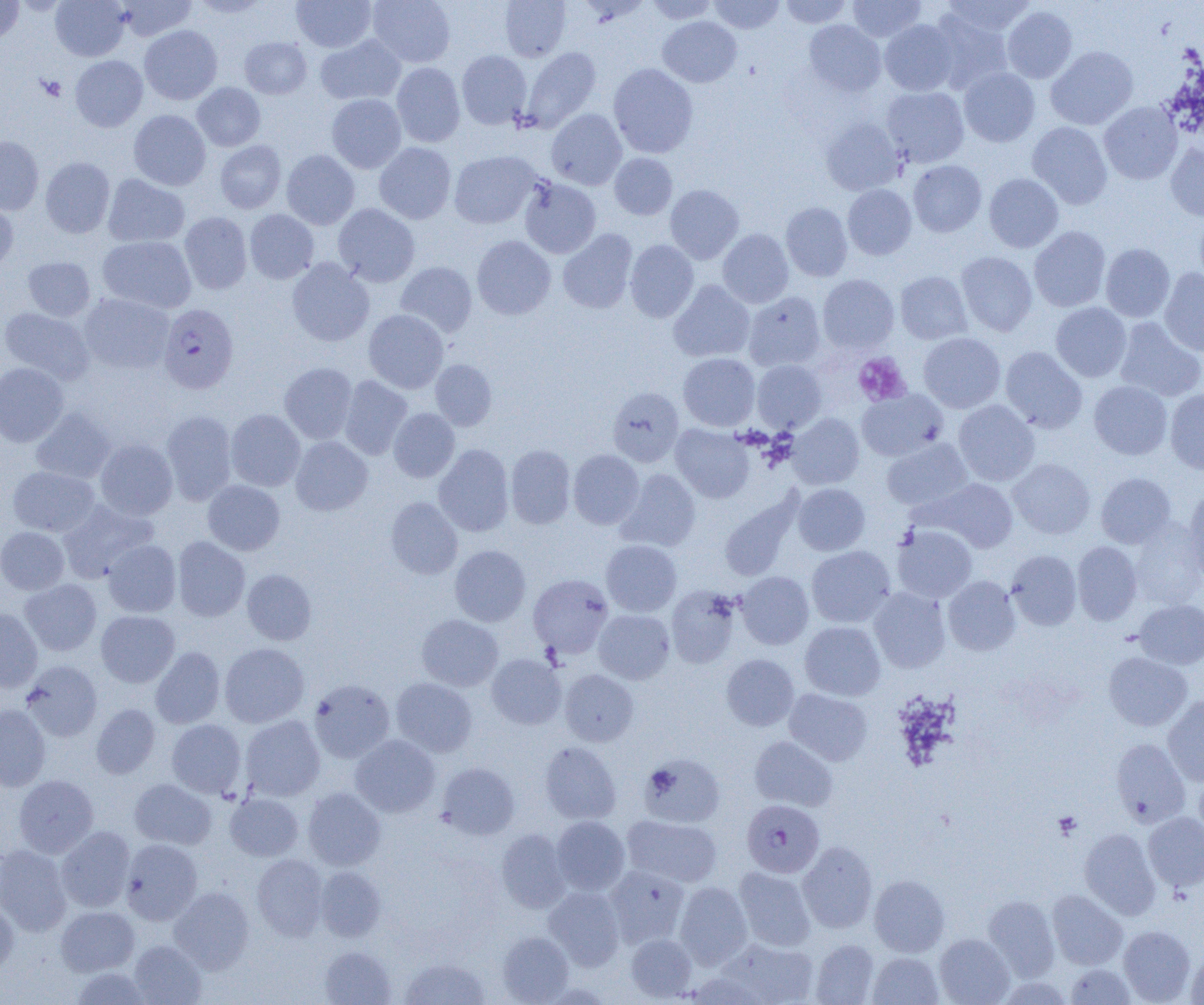

slide_level_diagnosis: Plasmodium falciparum
image_size: 1204×1005 pixels
preparation: thin blood film
modality: light microscopy
plasmodium_falciparum_infected_red_blood_cell_locations: 'approximate bounding boxes as (x1,y1)-(x2,y2) corner pairs in pixels: (158,304)-(239,394), (742,799)-(825,877)'
field_of_view: one of a larger specimen
magnification: 1000x
platelet_locations: 'approximate bounding boxes as (x1,y1)-(x2,y2) corner pairs in pixels: (38,76)-(67,101), (852,352)-(911,406), (1053,811)-(1082,839)'
uninfected_red_blood_cell_locations: 'approximate bounding boxes as (x1,y1)-(x2,y2) corner pairs in pixels: (50,0)-(130,61), (191,0)-(271,18), (292,0)-(376,52), (368,0)-(455,67), (499,0)-(571,61), (645,0)-(718,24), (708,0)-(785,34), (779,0)-(853,28), (848,0)-(926,42), (941,0)-(1036,37), (0,1)-(24,44), (115,1)-(197,41), (1002,6)-(1078,83), (928,10)-(1014,94), (658,16)-(742,87), (879,19)-(960,95), (803,20)-(886,96), (139,25)-(222,105), (315,34)-(406,105), (240,37)-(312,99), (1046,46)-(1138,130), (519,47)-(601,133), (456,50)-(532,129), (70,55)-(147,131), (391,62)-(466,147), (608,63)-(698,158), (959,68)-(1040,146), (192,83)-(265,151), (882,86)-(969,167), (326,94)-(407,173), (1099,101)-(1183,184), (546,109)-(627,189), (129,110)-(211,190), (821,117)-(904,195), (1027,122)-(1112,209), (0,136)-(44,215), (215,140)-(286,213), (374,142)-(456,224), (1165,143)-(1204,221), (281,150)-(359,229), (449,151)-(542,229), (609,153)-(677,220), (40,157)-(115,238), (908,160)-(987,237), (984,173)-(1064,253), (103,174)-(189,247), (519,178)-(601,258), (665,184)-(744,264), (843,184)-(916,260), (0,200)-(18,275), (781,202)-(853,282), (333,203)-(420,287), (244,209)-(319,284), (1193,210)-(1204,290), (180,212)-(252,294), (1029,227)-(1111,312), (558,229)-(638,313), (718,229)-(794,308), (472,235)-(556,320), (98,236)-(197,313), (625,240)-(699,323), (1100,243)-(1175,321), (956,251)-(1038,336), (23,257)-(95,321), (287,258)-(374,346), (395,261)-(478,338), (1159,268)-(1204,356), (895,271)-(972,345), (818,274)-(899,354), (669,281)-(755,362), (744,291)-(825,371), (79,293)-(174,374), (1050,302)-(1131,382), (0,307)-(94,384), (364,310)-(448,393), (1114,317)-(1204,402), (919,332)-(1005,413), (1000,346)-(1087,433), (678,353)-(760,431), (430,360)-(497,431), (752,360)-(827,432), (0,362)-(68,447), (280,362)-(357,444), (339,375)-(413,460), (1089,380)-(1173,460), (608,386)-(684,466), (1165,388)-(1204,474), (857,389)-(948,461), (953,400)-(1039,486), (31,407)-(117,484), (388,408)-(459,482), (226,409)-(305,491), (161,410)-(237,505), (787,413)-(864,489), (671,424)-(754,503), (290,436)-(373,515), (96,438)-(177,519), (882,438)-(973,511), (434,444)-(514,536), (506,444)-(576,529), (568,449)-(644,529), (1008,458)-(1095,539), (8,466)-(100,536), (617,469)-(701,551), (1096,472)-(1176,548), (923,478)-(1018,552), (203,480)-(285,555), (792,483)-(870,555), (1182,487)-(1204,581), (719,494)-(802,582), (385,497)-(463,579), (58,499)-(159,582), (1129,522)-(1203,610), (892,525)-(977,602), (0,527)-(69,594), (173,536)-(250,621), (103,539)-(181,617), (601,540)-(682,616), (1072,541)-(1142,625), (450,545)-(531,626), (806,545)-(896,628), (1006,549)-(1082,630), (242,569)-(316,645), (736,571)-(814,649), (528,573)-(613,657), (943,576)-(1021,655), (20,579)-(102,656), (666,586)-(741,668), (869,587)-(950,673), (1134,599)-(1204,669), (0,608)-(42,692), (593,609)-(675,684), (96,610)-(179,687), (417,614)-(503,691), (800,621)-(885,700), (220,643)-(309,728), (151,646)-(225,728), (1103,652)-(1192,730), (486,653)-(566,729), (721,654)-(799,731), (20,660)-(103,741), (560,669)-(639,746), (391,677)-(477,757), (309,679)-(395,762), (784,688)-(872,766), (1162,695)-(1204,786), (0,704)-(50,791), (91,704)-(160,778), (241,715)-(325,801), (167,719)-(246,798), (350,735)-(440,817), (749,736)-(838,811), (1110,737)-(1190,826), (539,741)-(621,824), (640,753)-(725,827), (437,763)-(519,840), (1194,771)-(1204,846), (14,775)-(98,858), (129,778)-(216,849), (303,787)-(386,870), (225,793)-(303,861), (1143,812)-(1204,892), (622,815)-(723,887), (551,816)-(630,895), (56,826)-(135,912), (1080,828)-(1161,919), (497,829)-(571,912), (122,839)-(202,925), (797,841)-(877,933), (0,845)-(72,936), (252,854)-(329,940), (604,865)-(690,948), (315,866)-(386,941), (734,866)-(816,951), (869,874)-(950,957), (674,881)-(752,969), (544,886)-(625,970), (169,887)-(255,973), (1047,890)-(1127,970), (983,895)-(1060,979), (0,897)-(19,976), (56,906)-(140,976), (1118,925)-(1195,1004), (497,931)-(574,1004), (625,933)-(697,1001), (934,933)-(1014,1005), (718,937)-(819,1004), (810,939)-(879,1004), (129,940)-(206,1005), (319,946)-(396,1005), (1186,948)-(1204,1005), (867,952)-(943,1005), (399,957)-(491,1004), (1065,963)-(1136,1004), (71,967)-(151,1004)'